Assess for Plasmodium parasites.
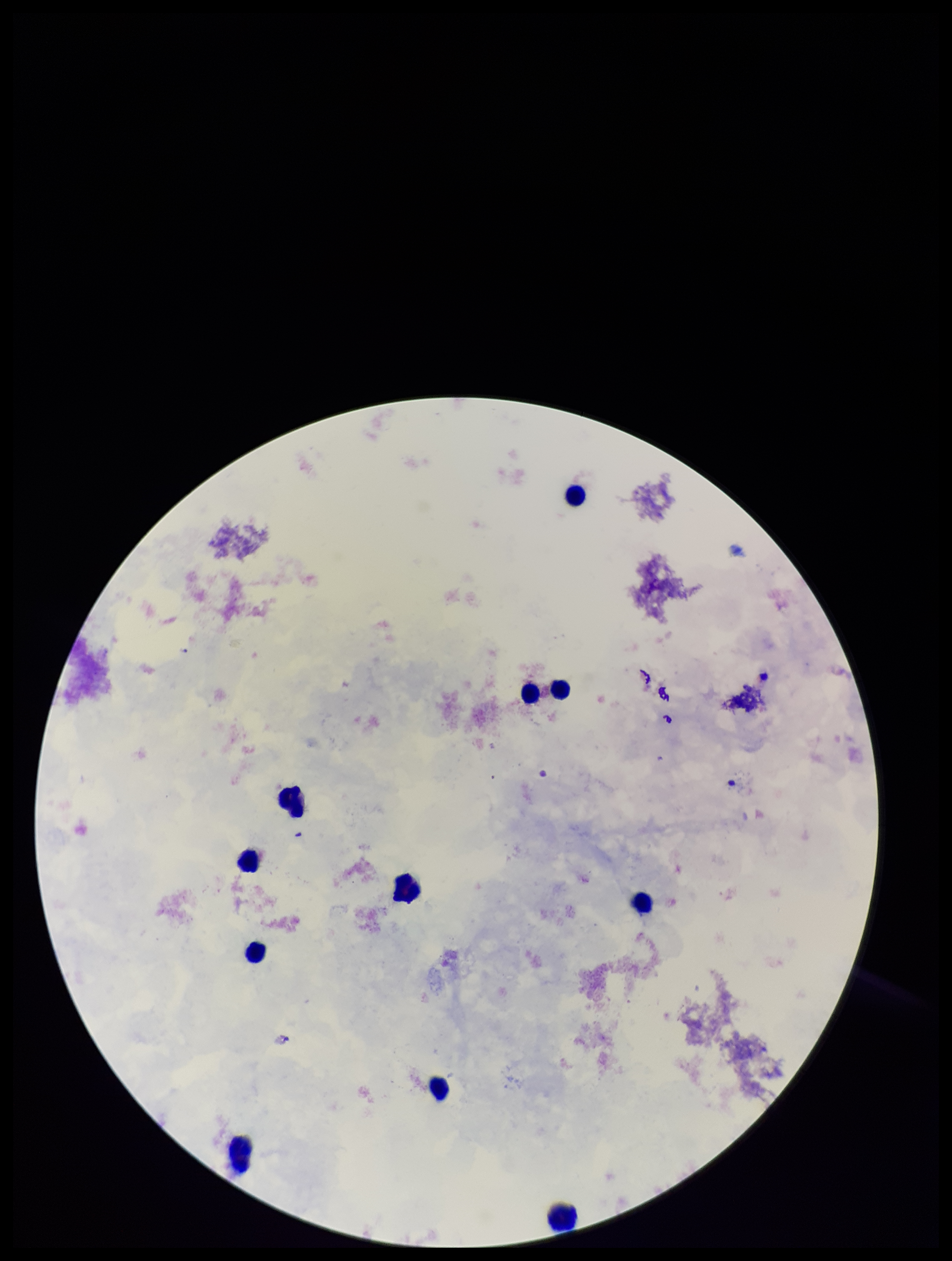
None identified.

Giemsa stain. One field from this slide. Parasite count: 0. Patient malaria status: negative. Image is 952×1261 pixels. Preparation: thick blood smear. Smartphone photograph taken through the eyepiece of a microscope. Leukocyte count: 11.